Give the extent of all Plasmodium malariae-infected red blood cells.
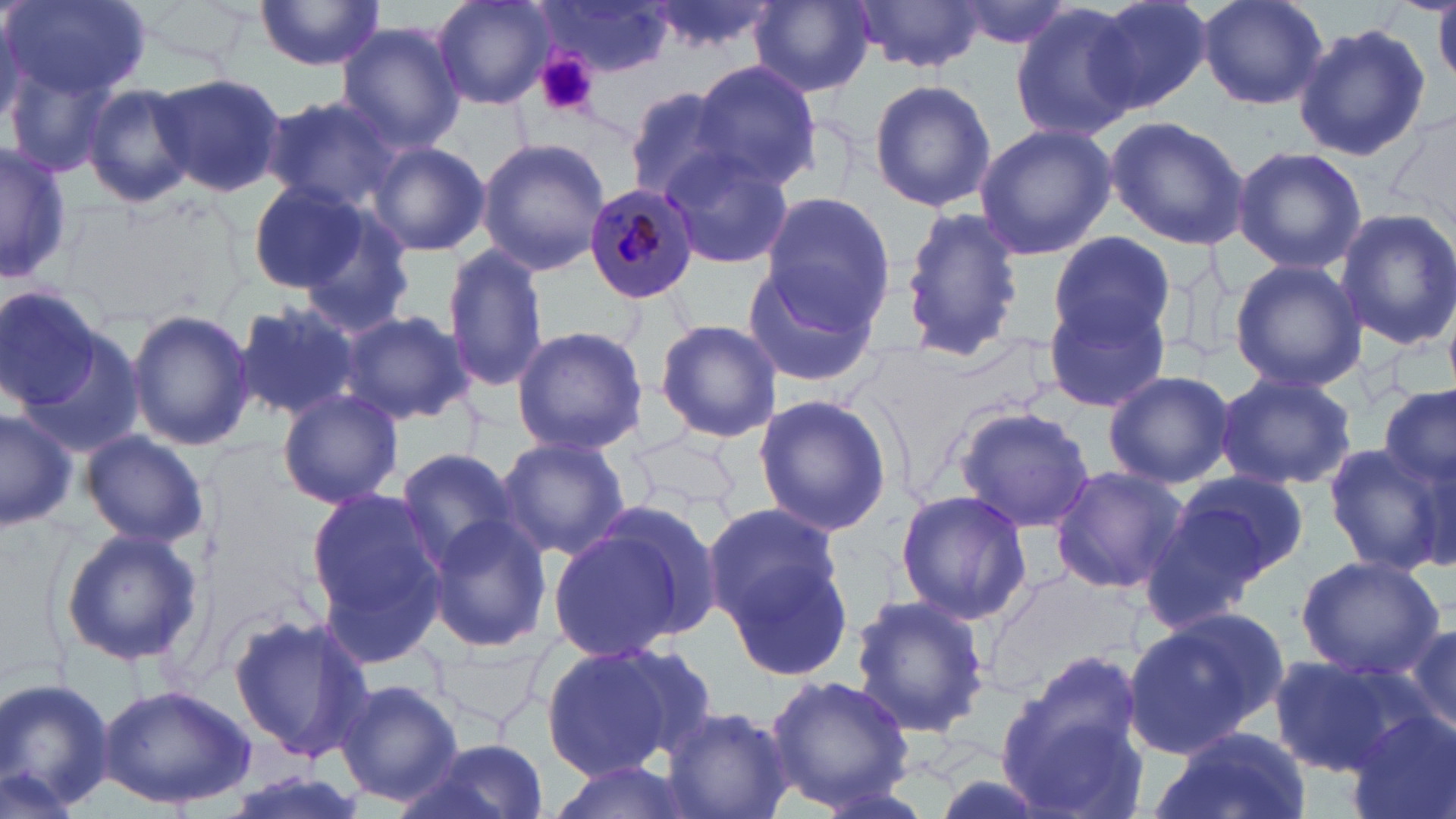

Approximate bounding boxes as (x1,y1)-(x2,y2) corner pairs in pixels.
Plasmodium malariae-infected red blood cells: (581,180)-(700,306).

{
  "slide_level_diagnosis": "Plasmodium malariae",
  "modality": "light microscopy",
  "platelet_locations": "approximate bounding boxes as (x1,y1)-(x2,y2) corner pairs in pixels: (534,53)-(599,116)",
  "preparation": "thin blood smear",
  "uninfected_red_blood_cell_locations": "approximate bounding boxes as (x1,y1)-(x2,y2) corner pairs in pixels: (6,0)-(150,100), (253,0)-(386,71), (433,0)-(555,109), (851,0)-(987,75), (949,0)-(1078,49), (1089,0)-(1214,118), (1196,0)-(1330,111), (541,1)-(677,77), (749,1)-(874,97), (1009,4)-(1140,141), (1291,22)-(1430,163), (335,23)-(466,151), (6,61)-(115,177), (691,61)-(820,189), (152,71)-(287,199), (868,78)-(995,212), (78,83)-(198,208), (622,87)-(741,202), (260,94)-(406,213), (1383,111)-(1456,248), (1104,116)-(1250,249), (973,123)-(1116,260), (477,138)-(610,276), (368,141)-(491,258), (0,143)-(71,286), (658,145)-(795,271), (1231,145)-(1367,276), (243,179)-(378,302), (761,191)-(895,325), (291,204)-(417,338), (899,207)-(1023,363), (1333,207)-(1456,352), (1049,230)-(1174,346), (444,243)-(548,394), (1228,258)-(1365,393), (738,262)-(881,391), (0,285)-(104,408), (1042,289)-(1171,416), (233,299)-(361,422), (125,309)-(257,450), (337,311)-(473,425), (654,319)-(783,442), (510,324)-(647,456), (17,327)-(150,461), (1102,369)-(1236,489), (1214,371)-(1357,492), (1378,383)-(1456,492), (276,390)-(404,509), (753,393)-(893,536), (953,405)-(1095,533), (0,407)-(78,533), (77,429)-(210,549), (499,435)-(630,561), (1320,443)-(1450,573), (394,448)-(523,575), (1049,466)-(1188,594), (1169,470)-(1313,585), (1135,487)-(1283,634), (305,489)-(452,657), (893,489)-(1031,624), (555,501)-(721,657), (705,503)-(854,682), (425,515)-(552,651), (59,527)-(202,666), (1294,553)-(1446,680), (985,565)-(1131,696), (848,593)-(991,738), (228,613)-(372,765), (1123,613)-(1275,753), (1396,618)-(1456,742), (430,639)-(547,726), (537,645)-(686,780), (997,651)-(1150,815), (1267,655)-(1404,775), (762,673)-(917,812), (0,675)-(117,818), (334,678)-(463,808), (97,685)-(256,812), (661,704)-(795,819), (1348,712)-(1456,819), (1153,728)-(1312,819), (399,739)-(549,819), (543,758)-(698,818)",
  "image_size": "1456×819 pixels",
  "field_of_view": "single",
  "magnification": "1000x",
  "stain": "May-Grünwald-Giemsa"
}